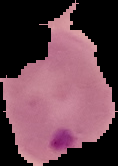
Summary:
  - Result: Plasmodium parasites identified
  - Image size: 118×166 pixels
  - Preparation: thin blood smear
  - Image type: segmented cell region on a black background